Classify this cell by malaria status.
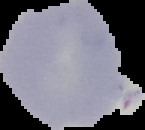

It is uninfected.

From a thin blood film. The area outside the segmented cell region is set to black. Image is 145×130 pixels.